Outline each blood parasite and name the species.
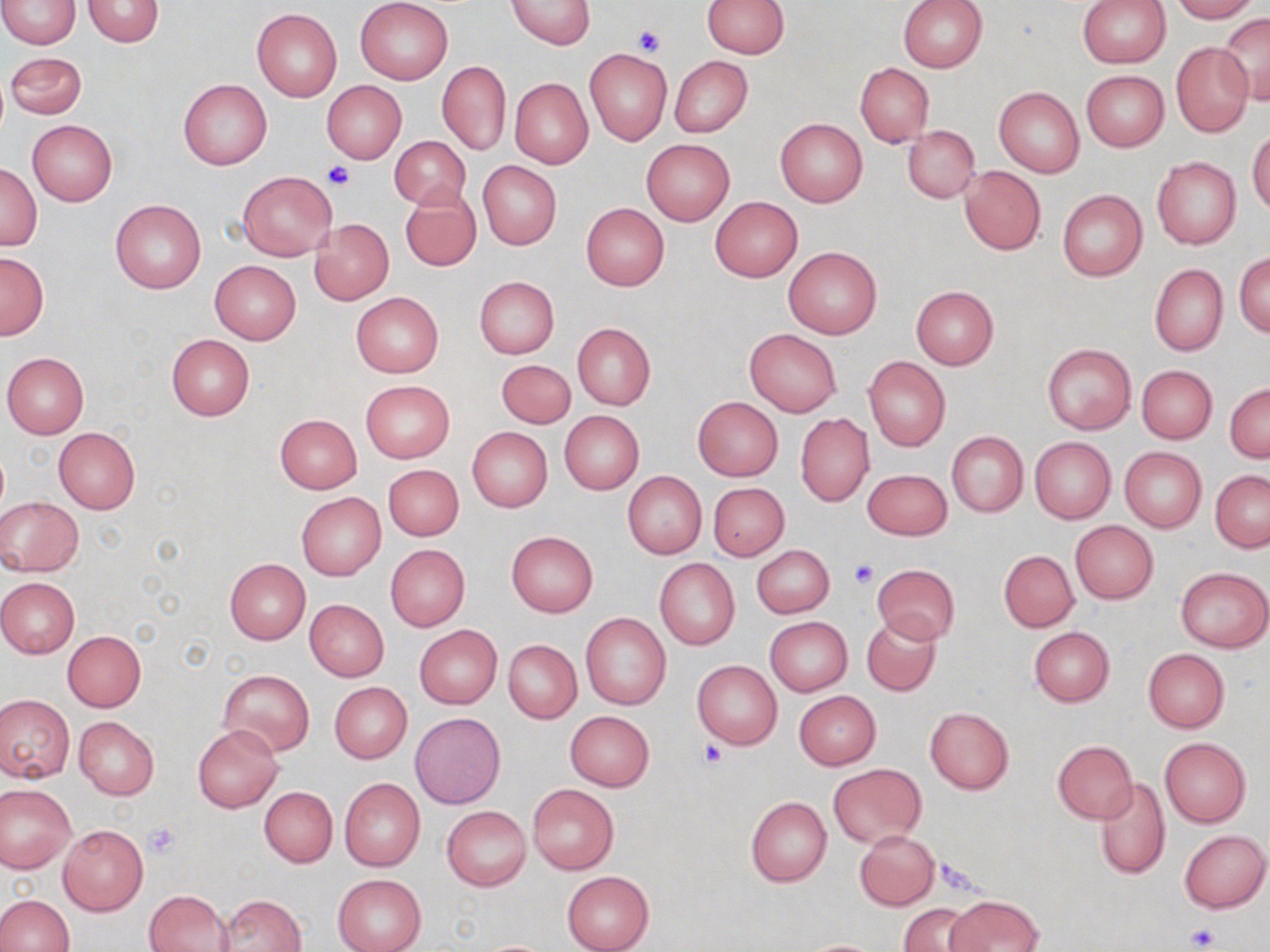

No blood parasites observed.

Approximate bounding boxes as (x1, y1, x2, y2) in pixels. Uninfected red blood cell locations: (0, 0, 81, 49), (82, 0, 163, 46), (355, 0, 453, 85), (508, 0, 594, 49), (702, 0, 789, 58), (898, 0, 987, 71), (1077, 0, 1170, 67), (1170, 0, 1257, 22), (251, 8, 342, 101), (1218, 13, 1270, 105), (1170, 43, 1254, 138), (584, 49, 671, 144), (5, 51, 88, 119), (669, 56, 752, 136), (438, 62, 510, 155), (854, 63, 934, 147), (1081, 70, 1169, 151), (509, 78, 593, 168), (179, 79, 271, 169), (322, 81, 407, 164), (994, 86, 1083, 177), (776, 118, 867, 207), (28, 120, 117, 205), (902, 125, 980, 202), (1247, 128, 1270, 214), (389, 134, 472, 212), (641, 138, 734, 225), (1151, 155, 1241, 250), (477, 161, 562, 250), (1, 163, 42, 250), (958, 166, 1046, 255), (238, 171, 335, 262), (402, 187, 481, 271), (1057, 190, 1147, 282), (710, 197, 802, 281), (111, 200, 205, 294), (581, 203, 669, 291), (308, 218, 393, 305), (782, 244, 882, 339), (0, 251, 49, 339), (1235, 252, 1270, 337), (210, 260, 301, 344), (1149, 263, 1227, 356), (474, 277, 559, 358), (911, 286, 999, 370), (351, 292, 443, 377), (572, 323, 656, 410), (744, 329, 841, 417), (166, 334, 255, 421), (1041, 342, 1136, 435), (1, 352, 90, 438), (864, 356, 950, 451), (497, 360, 575, 428), (1136, 365, 1217, 444), (360, 380, 455, 463), (1225, 382, 1269, 462), (693, 397, 782, 480), (559, 410, 644, 496), (275, 414, 362, 493), (795, 414, 873, 507), (467, 427, 553, 513), (53, 428, 140, 515), (947, 432, 1028, 517), (1030, 438, 1116, 523), (1119, 447, 1206, 532), (383, 464, 463, 540), (863, 469, 952, 540), (622, 471, 707, 559), (1210, 471, 1270, 552), (708, 482, 790, 561), (296, 493, 386, 580), (0, 497, 84, 576), (1070, 521, 1158, 603), (506, 531, 598, 616), (385, 544, 470, 631), (752, 545, 835, 618), (999, 550, 1078, 632), (224, 559, 310, 644), (655, 560, 740, 649), (872, 564, 960, 643), (1176, 566, 1269, 652), (0, 577, 80, 658), (304, 598, 389, 681), (580, 612, 672, 711), (861, 614, 942, 697), (765, 616, 852, 696), (414, 625, 502, 708), (1028, 626, 1115, 706), (62, 630, 146, 711), (504, 640, 581, 723), (1143, 649, 1229, 732), (692, 659, 782, 749), (218, 669, 314, 756), (329, 682, 412, 764), (794, 691, 880, 769), (1, 694, 74, 782), (925, 707, 1014, 795), (564, 710, 654, 791), (410, 713, 505, 808), (74, 716, 159, 799), (193, 724, 283, 811), (1160, 738, 1251, 827), (1053, 741, 1138, 823), (829, 764, 925, 847), (1095, 776, 1170, 879), (340, 778, 425, 870), (527, 783, 618, 875), (0, 784, 76, 872), (260, 786, 337, 867), (746, 796, 832, 888), (441, 805, 531, 891), (57, 825, 148, 915), (854, 829, 939, 910), (1180, 829, 1269, 913), (562, 871, 654, 952), (333, 874, 426, 952), (145, 889, 233, 951), (0, 894, 74, 951), (218, 894, 307, 952), (946, 895, 1042, 952), (899, 902, 975, 952), (796, 938, 887, 951). Platelet locations: (631, 26, 666, 57), (323, 161, 354, 191), (849, 559, 878, 588), (698, 741, 729, 768), (144, 822, 180, 858), (1187, 924, 1218, 950). Slide-level diagnosis: negative for blood parasites. Light microscopy. Thin blood smear. May-Grünwald-Giemsa-stained preparation. Single field of view. 1000x magnification. Image is 1270×952 pixels.